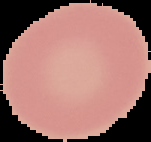

preparation = thin blood smear
malaria status = uninfected
image type = segmented cell region on a black background
image size = 151×142 pixels